Report the malaria status of this cell.
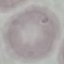

Uninfected.

capture = smartphone through the microscope eyepiece
image type = automatically extracted cell patch, resized to 64 × 64 pixels
preparation = thin blood smear
stain = Giemsa